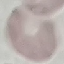
{
  "malaria_status": "uninfected",
  "image_type": "cell patch, automatically extracted from a larger field of view and resized to 64 × 64 pixels",
  "stain": "Giemsa",
  "preparation": "thin blood smear",
  "capture": "smartphone camera at the microscope eyepiece"
}